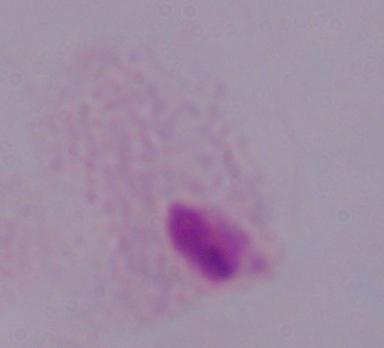

magnification: 1000x
modality: photomicrograph
identification: trichomonad